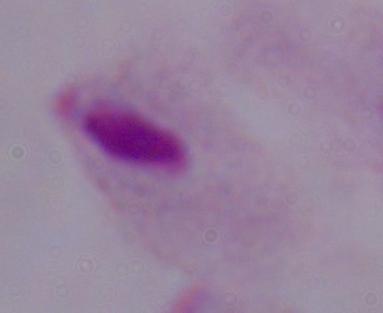

magnification = 1000x
identification = trichomonad
modality = micrograph